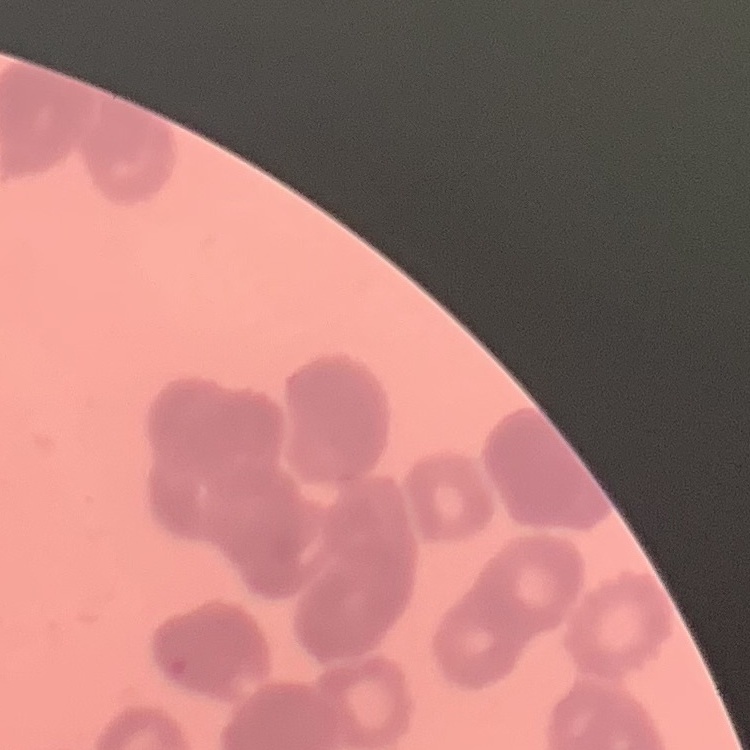
{
  "red_blood_cell_morphology": "rouleaux formation",
  "preparation": "thin peripheral smear",
  "image_type": "square crop of a larger photomicrograph",
  "stain": "Field's or Giemsa"
}